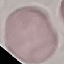 Malaria status: uninfected. Acquired by smartphone through the microscope eyepiece. Giemsa-stained preparation. Cell patch, automatically extracted from a larger field of view and resized to 64 × 64 pixels. Thin blood film.